Classify this cell by malaria status.
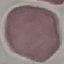

It is uninfected.

{
  "image_type": "automatically extracted cell patch, resized to 64 × 64 pixels",
  "stain": "Giemsa",
  "capture": "smartphone through the microscope eyepiece",
  "preparation": "thin blood smear"
}